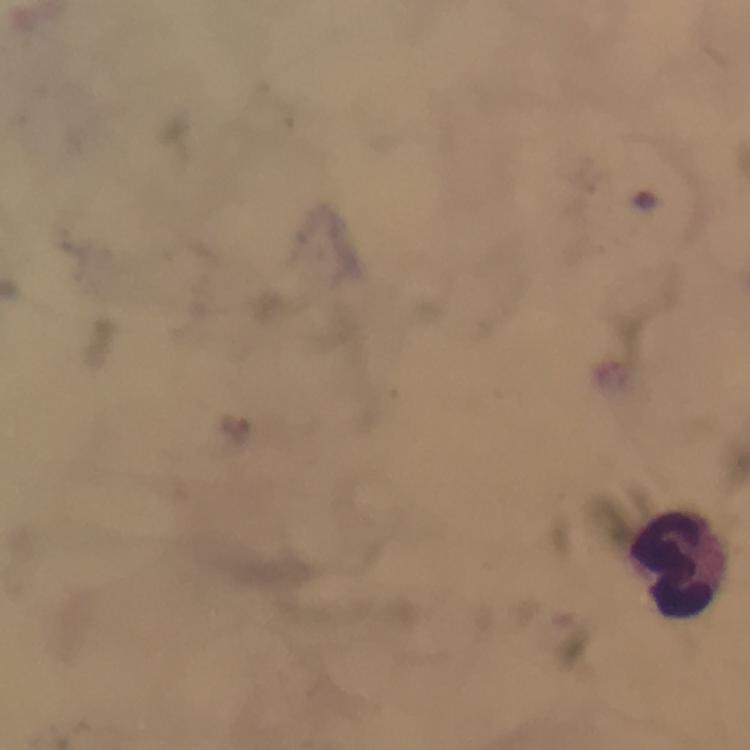
Approximate centers as [x, y] in pixels.
Summary:
  - Leukocyte locations: [684, 566]
  - Plasmodium parasite locations: [235, 427]
  - Magnification: 100x
  - Stain: Giemsa
  - Cropped from: one field of view
  - Preparation: thick blood film
  - Image size: 750×750 pixels
  - Context: from a diagnostic examination for malaria
  - Capture: smartphone camera through the microscope
  - Immersion oil: applied